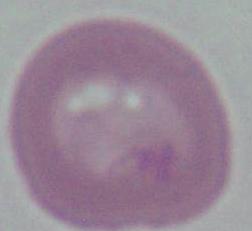

A red blood cell is seen. Captured at 1000x magnification. Photomicrograph.